Identify the parasite.
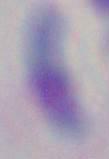
This is Toxoplasma gondii.

Summary:
  - Modality: micrograph
  - Magnification: 1000x